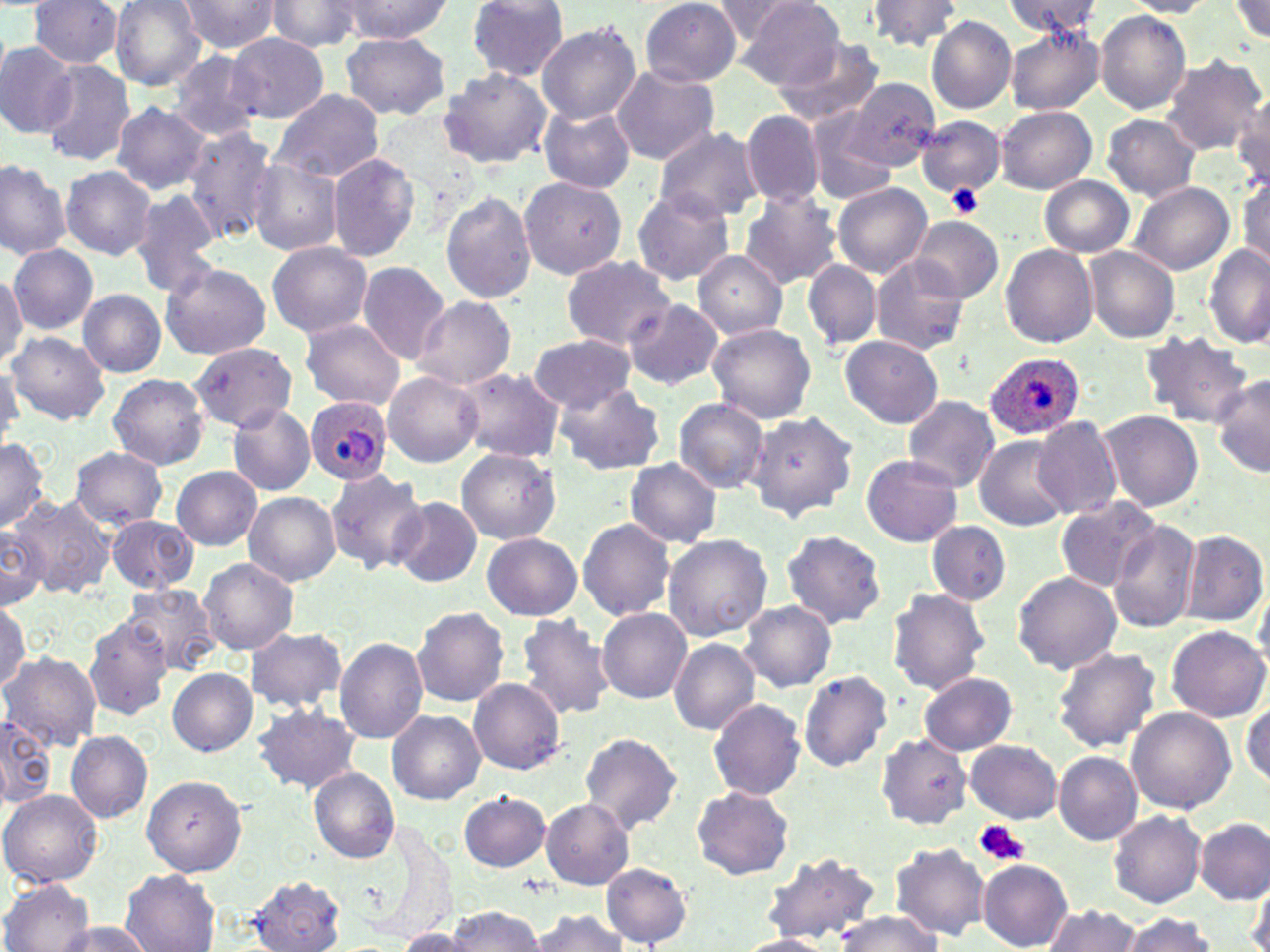 Approximate bounding boxes as (x1, y1, x2, y2) in pixels. Uninfected red blood cell locations: (28, 0, 123, 68), (109, 0, 209, 89), (267, 0, 365, 53), (705, 0, 804, 43), (739, 0, 849, 89), (1001, 0, 1106, 38), (1228, 0, 1269, 46), (175, 1, 283, 52), (337, 1, 451, 41), (466, 1, 570, 80), (641, 1, 742, 85), (865, 1, 964, 53), (1120, 1, 1218, 16), (1095, 11, 1192, 113), (927, 16, 1015, 114), (536, 22, 640, 124), (1004, 24, 1104, 115), (341, 32, 450, 119), (227, 33, 328, 121), (775, 36, 885, 128), (0, 44, 76, 139), (166, 50, 265, 142), (1160, 54, 1268, 156), (39, 61, 134, 166), (611, 65, 719, 164), (439, 67, 551, 169), (842, 76, 941, 174), (268, 89, 384, 183), (1233, 92, 1269, 194), (113, 102, 210, 195), (538, 104, 636, 194), (996, 105, 1096, 194), (804, 109, 901, 206), (742, 110, 824, 207), (1102, 113, 1201, 201), (915, 116, 1006, 199), (181, 126, 281, 243), (653, 127, 765, 222), (326, 152, 421, 263), (0, 158, 71, 262), (246, 158, 343, 256), (60, 166, 158, 260), (520, 176, 627, 279), (1040, 176, 1134, 258), (1236, 177, 1270, 274), (1129, 182, 1234, 276), (833, 183, 933, 278), (630, 188, 734, 285), (440, 189, 536, 304), (737, 189, 841, 288), (127, 190, 221, 294), (908, 216, 1004, 305), (266, 243, 373, 337), (9, 244, 98, 333), (1000, 244, 1099, 347), (1203, 244, 1268, 348), (1085, 247, 1179, 343), (693, 250, 788, 339), (872, 256, 969, 357), (562, 257, 676, 348), (160, 260, 272, 360), (804, 260, 880, 349), (357, 262, 449, 364), (0, 267, 27, 366), (79, 290, 165, 376), (411, 296, 517, 390), (620, 298, 724, 391), (299, 318, 405, 411), (707, 322, 817, 424), (7, 330, 109, 423), (1141, 331, 1255, 428), (529, 334, 636, 413), (840, 335, 944, 428), (190, 342, 296, 433), (0, 365, 22, 452), (456, 367, 564, 463), (383, 372, 485, 467), (106, 373, 210, 470), (1211, 374, 1270, 478), (554, 382, 664, 475), (900, 394, 1000, 493), (672, 398, 769, 493), (227, 403, 314, 497), (1099, 410, 1204, 514), (748, 411, 860, 522), (1032, 416, 1123, 519), (974, 434, 1072, 531), (0, 439, 51, 531), (71, 447, 167, 528), (457, 448, 560, 545), (862, 454, 963, 547), (624, 457, 723, 548), (324, 466, 426, 575), (171, 467, 261, 550), (243, 492, 341, 585), (7, 494, 116, 600), (390, 496, 481, 587), (1054, 496, 1160, 591), (106, 514, 196, 592), (577, 518, 675, 620), (927, 520, 1010, 605), (1109, 520, 1201, 635), (0, 522, 49, 608), (781, 530, 887, 629), (1183, 531, 1266, 626), (482, 533, 582, 620), (662, 534, 772, 641), (199, 557, 298, 655), (1012, 571, 1122, 674), (1254, 581, 1270, 667), (123, 584, 219, 677), (887, 588, 989, 693), (0, 596, 30, 694), (740, 601, 836, 691), (411, 607, 509, 707), (597, 608, 692, 704), (515, 613, 614, 721), (84, 614, 173, 720), (1167, 625, 1268, 723), (244, 627, 349, 712), (335, 637, 429, 744), (670, 639, 760, 734), (1051, 645, 1161, 752), (2, 652, 101, 750), (168, 668, 256, 755), (798, 670, 892, 772), (918, 672, 1017, 755), (468, 677, 565, 774), (708, 698, 806, 801), (1243, 699, 1270, 789), (253, 701, 359, 793), (1126, 706, 1237, 813), (0, 711, 55, 807), (388, 711, 485, 803), (67, 730, 153, 823), (580, 730, 683, 834), (873, 733, 971, 827), (965, 739, 1062, 824), (1054, 752, 1143, 846), (310, 767, 400, 863), (141, 774, 248, 877), (691, 786, 794, 880), (1, 790, 102, 886), (458, 791, 552, 872), (542, 799, 633, 890), (1109, 810, 1205, 907), (1197, 818, 1269, 904), (890, 842, 989, 940), (763, 851, 882, 945), (979, 858, 1073, 951), (600, 863, 692, 946), (120, 869, 221, 951), (244, 875, 346, 952), (1249, 876, 1270, 952), (1, 877, 94, 952), (1042, 903, 1144, 952), (442, 907, 544, 952), (527, 910, 631, 951), (831, 910, 944, 952), (1121, 913, 1216, 952), (56, 920, 155, 952), (396, 927, 471, 950), (734, 934, 836, 952). Platelet locations: (949, 185, 981, 215), (974, 820, 1030, 866). Plasmodium ovale-infected red blood cell locations: (983, 352, 1086, 439), (306, 397, 395, 484). Slide-level diagnosis: Plasmodium ovale. May-Grünwald-Giemsa-stained preparation. Image is 1270×952 pixels. 1000x magnification. Optical microscopy. One field of a larger specimen. Thin blood smear.